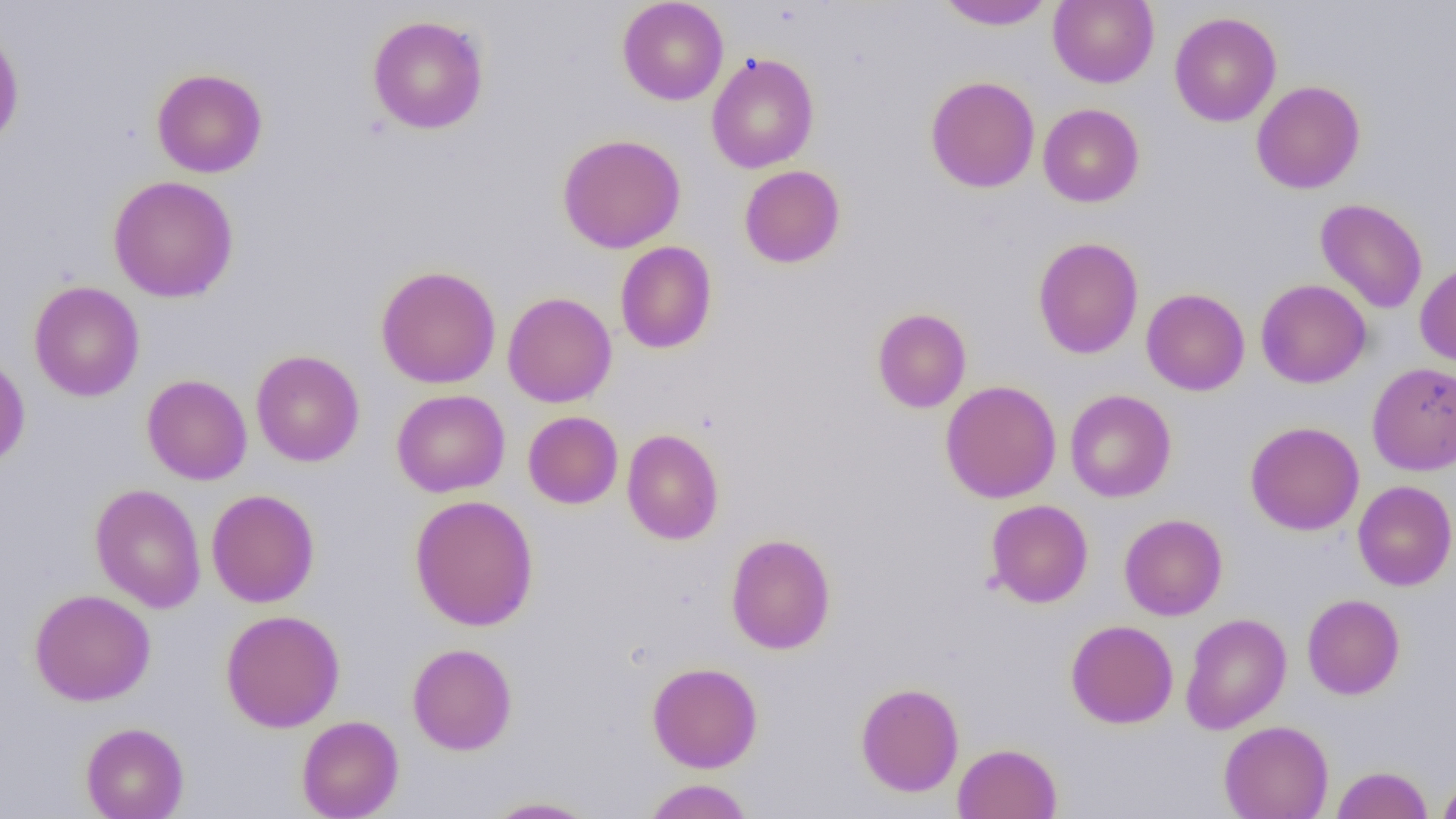
Summary:
  - Coordinate format: approximate bounding boxes as [x1, y1, x2, y2] in pixels
  - Uninfected red blood cell locations: [617, 0, 728, 105], [1048, 0, 1159, 88], [936, 1, 1055, 31], [1169, 11, 1282, 127], [367, 14, 489, 134], [0, 23, 25, 150], [706, 52, 819, 173], [151, 68, 268, 178], [925, 76, 1040, 193], [1252, 80, 1365, 194], [1038, 103, 1144, 207], [557, 134, 686, 253], [739, 165, 846, 268], [108, 175, 239, 302], [1315, 198, 1428, 314], [1032, 237, 1144, 359], [615, 241, 717, 354], [1415, 260, 1456, 368], [376, 265, 502, 389], [1255, 279, 1371, 388], [28, 281, 145, 402], [1141, 288, 1250, 396], [503, 291, 617, 408], [871, 308, 972, 413], [250, 350, 365, 467], [0, 352, 30, 469], [1367, 361, 1456, 475], [141, 374, 252, 485], [940, 380, 1061, 503], [391, 389, 510, 497], [1065, 389, 1176, 502], [523, 411, 623, 509], [1246, 421, 1364, 535], [622, 428, 724, 545], [1353, 480, 1456, 590], [90, 484, 206, 613], [206, 488, 320, 607], [409, 494, 539, 631], [985, 499, 1093, 608], [1119, 513, 1228, 620], [725, 533, 836, 654], [29, 588, 156, 706], [1302, 593, 1405, 699], [220, 609, 345, 732], [1180, 613, 1291, 734], [1066, 619, 1178, 728], [407, 643, 517, 755], [647, 662, 763, 773], [855, 681, 964, 797], [296, 715, 404, 819], [1219, 720, 1334, 819], [80, 722, 189, 819], [952, 742, 1062, 819], [1331, 765, 1433, 818], [1437, 772, 1456, 819], [641, 779, 755, 818], [484, 796, 600, 818]
  - Slide-level diagnosis: no evidence of blood parasites
  - Modality: light microscopy
  - Magnification: 1000x
  - Field of view: single
  - Preparation: thin blood smear
  - Image size: 1456×819 pixels